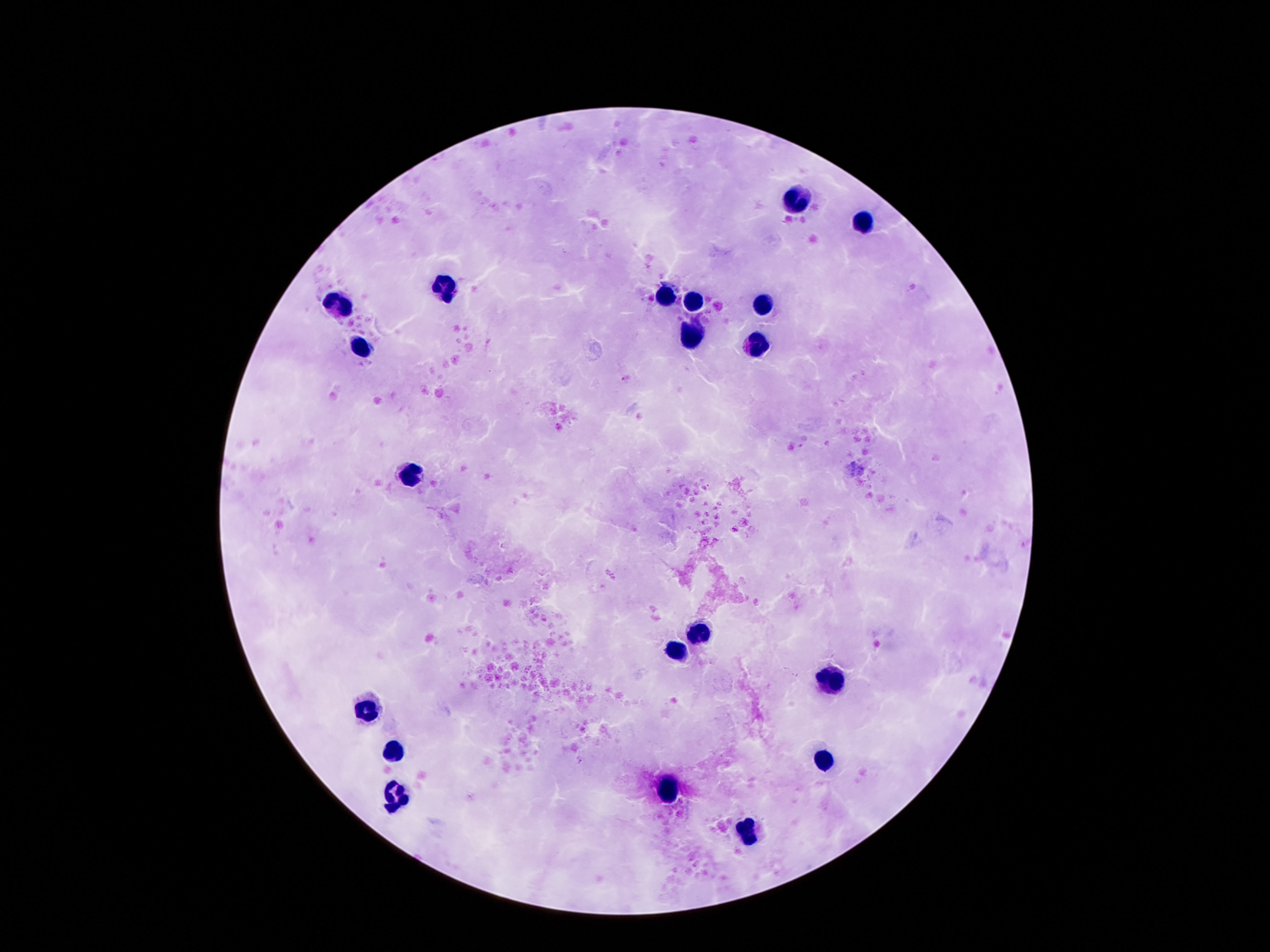 Approximate object centers, in pixels from the top-left corner. Leukocyte locations: (x=795, y=203), (x=860, y=224), (x=445, y=288), (x=663, y=297), (x=764, y=301), (x=692, y=304), (x=340, y=306), (x=692, y=339), (x=363, y=347), (x=760, y=348), (x=413, y=474), (x=697, y=632), (x=673, y=652), (x=829, y=681), (x=369, y=707), (x=392, y=755), (x=820, y=763), (x=667, y=791), (x=394, y=800), (x=747, y=833). 100x magnification. Single field of view. Patient malaria status: not infected. Giemsa-stained preparation. Image is 1270×952 pixels. Thick peripheral-blood smear. Photographed through the microscope eyepiece with a smartphone camera.